Comment on the morphology of the erythrocytes.
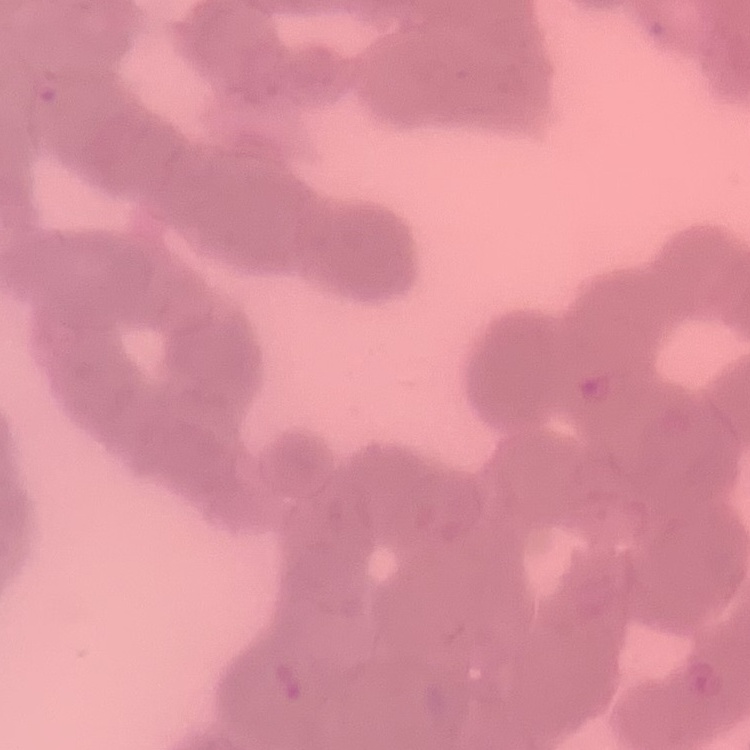
Rouleaux formation.

Summary:
  - Image type: square crop of a larger photomicrograph
  - Preparation: thin peripheral smear
  - Stain: Field's or Giemsa